State the blood parasite species.
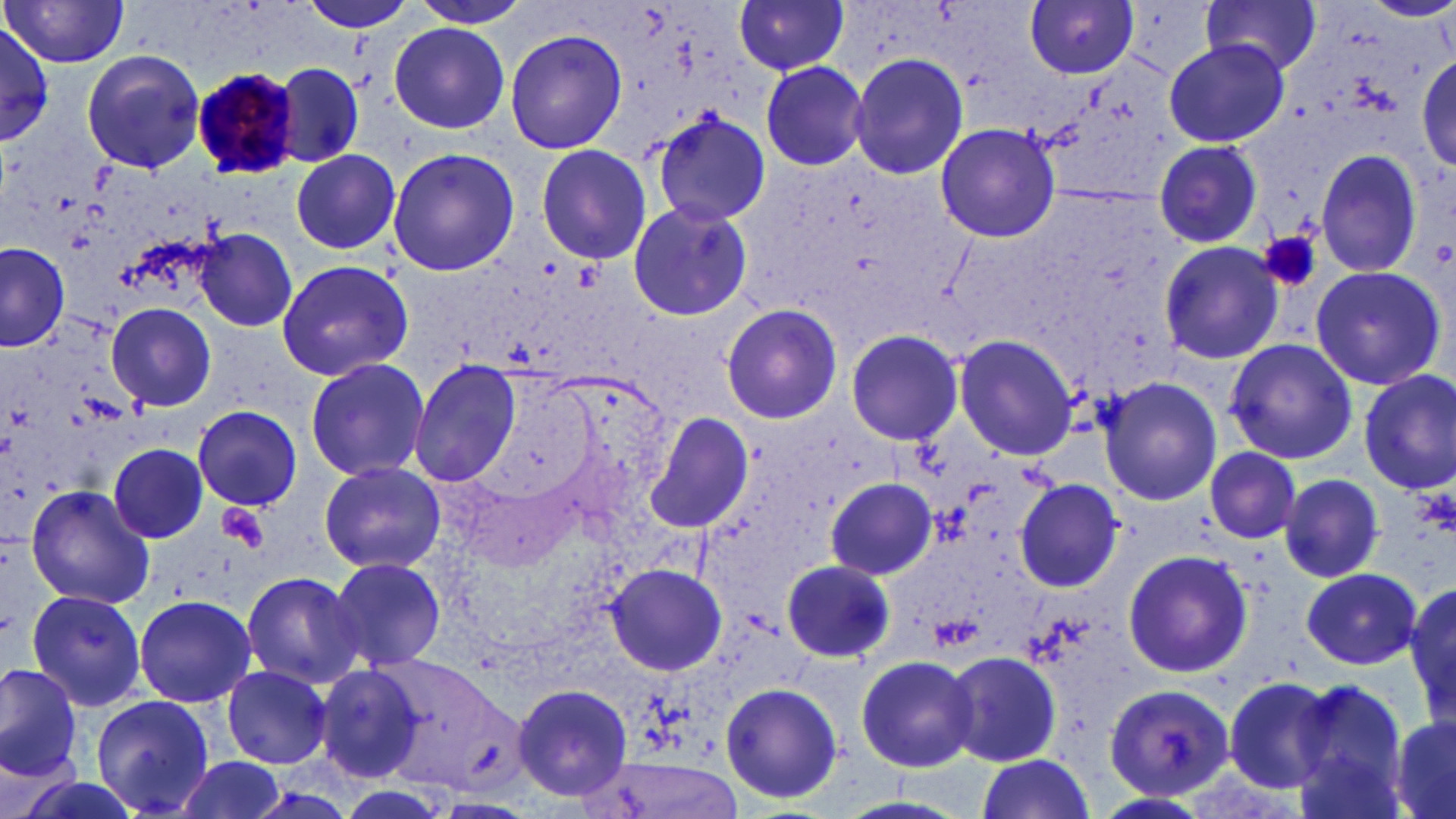

Plasmodium malariae.

Approximate bounding boxes as [x1, y1, x2, y2] in pixels. Plasmodium malariae-infected red blood cell locations: [189, 66, 298, 179]. Uninfected red blood cell locations: [406, 0, 533, 30], [1201, 0, 1322, 77], [298, 1, 420, 34], [734, 1, 850, 76], [1026, 1, 1138, 78], [3, 2, 129, 67], [0, 21, 55, 147], [389, 22, 510, 133], [503, 28, 627, 156], [1164, 40, 1288, 148], [79, 49, 207, 173], [846, 53, 969, 178], [1416, 53, 1456, 172], [273, 61, 364, 167], [281, 61, 379, 253], [760, 62, 870, 170], [653, 113, 773, 224], [935, 122, 1061, 244], [1153, 138, 1263, 248], [534, 144, 652, 264], [387, 148, 519, 278], [1314, 148, 1425, 278], [291, 150, 401, 254], [625, 201, 753, 321], [196, 229, 298, 331], [0, 242, 71, 351], [1160, 242, 1284, 363], [276, 259, 413, 381], [1308, 265, 1445, 390], [107, 303, 216, 411], [721, 303, 843, 424], [845, 330, 964, 448], [953, 334, 1078, 460], [1224, 337, 1358, 465], [304, 357, 431, 483], [408, 360, 522, 486], [1357, 368, 1456, 495], [1097, 375, 1222, 505], [192, 405, 301, 510], [646, 413, 755, 533], [108, 442, 211, 544], [1204, 446, 1301, 544], [319, 461, 444, 572], [1279, 474, 1384, 583], [827, 478, 940, 580], [1013, 478, 1123, 591], [24, 485, 156, 610], [1122, 548, 1253, 679], [327, 556, 446, 672], [782, 559, 894, 663], [606, 563, 727, 675], [1301, 567, 1422, 669], [238, 569, 365, 688], [1406, 580, 1456, 723], [25, 587, 149, 713], [133, 594, 257, 709], [945, 651, 1063, 766], [855, 654, 979, 771], [372, 656, 522, 792], [0, 662, 85, 782], [221, 665, 332, 768], [316, 665, 429, 784], [1223, 677, 1339, 793], [1287, 679, 1412, 815], [512, 681, 633, 803], [720, 681, 844, 805], [1105, 684, 1236, 799], [88, 695, 216, 816], [1388, 715, 1456, 819], [972, 755, 1096, 819], [172, 756, 290, 819], [598, 759, 748, 816], [1095, 792, 1213, 817]. Platelet locations: [1259, 231, 1321, 293], [1412, 481, 1454, 537], [218, 504, 269, 553]. Captured at 1000x magnification. Single field of view. Thin blood film. Light microscopy. Image is 1456×819 pixels. May-Grünwald-Giemsa stain.